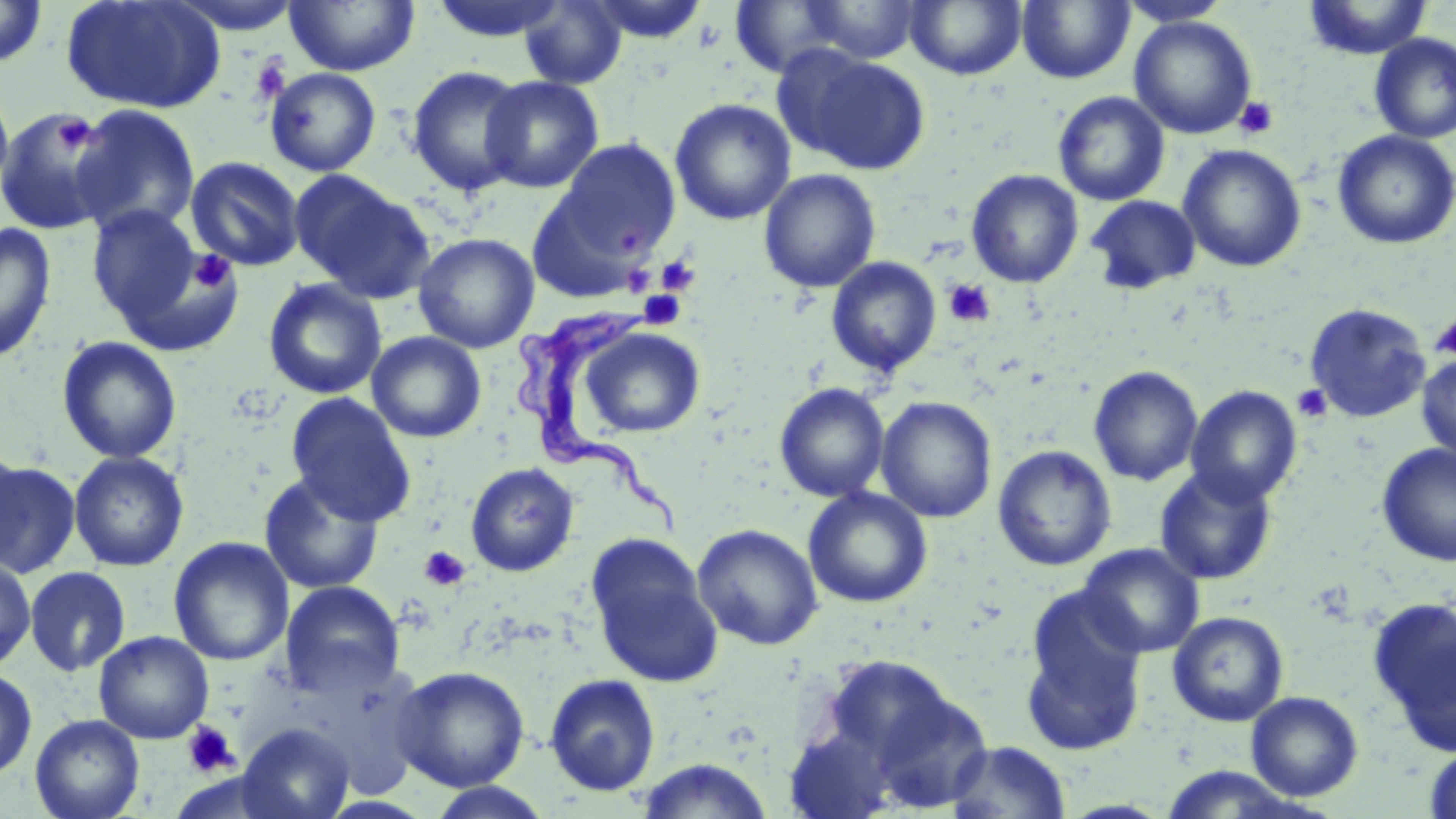
Approximate bounding boxes as [x1, y1, x2, y2] in pixels. Platelet locations: [250, 54, 290, 104], [1234, 96, 1279, 139], [52, 113, 95, 153], [188, 249, 237, 293], [655, 255, 700, 296], [943, 277, 995, 328], [638, 290, 687, 330], [1429, 314, 1456, 360], [1292, 384, 1332, 423], [420, 546, 471, 591], [181, 720, 239, 777]. Uninfected red blood cell locations: [167, 0, 305, 34], [285, 0, 419, 76], [428, 0, 568, 43], [585, 0, 710, 43], [905, 0, 1026, 80], [1116, 0, 1233, 26], [1303, 0, 1433, 60], [0, 1, 48, 68], [61, 1, 225, 115], [519, 1, 627, 89], [800, 1, 924, 63], [1017, 1, 1134, 84], [729, 2, 846, 78], [1129, 15, 1257, 139], [1369, 33, 1456, 143], [792, 50, 930, 175], [406, 65, 529, 197], [265, 67, 381, 176], [479, 75, 604, 193], [0, 80, 14, 203], [1052, 91, 1170, 207], [669, 98, 797, 225], [69, 104, 201, 238], [0, 107, 118, 234], [1333, 130, 1456, 250], [555, 138, 682, 261], [1178, 144, 1307, 272], [185, 156, 305, 271], [758, 169, 881, 293], [291, 170, 436, 304], [966, 170, 1083, 288], [1086, 195, 1201, 295], [86, 206, 222, 339], [0, 222, 58, 364], [413, 232, 540, 353], [826, 256, 942, 377], [263, 278, 387, 400], [1303, 302, 1432, 423], [580, 326, 705, 437], [366, 331, 486, 443], [56, 335, 182, 464], [1415, 352, 1456, 464], [1088, 366, 1203, 486], [773, 382, 890, 502], [1186, 385, 1303, 507], [285, 392, 416, 525], [876, 396, 998, 523], [0, 440, 28, 569], [1377, 442, 1456, 566], [993, 444, 1116, 571], [68, 451, 189, 572], [1, 460, 82, 579], [465, 462, 579, 577], [1153, 465, 1278, 585], [258, 472, 385, 594], [802, 487, 933, 608], [692, 523, 824, 650], [168, 537, 294, 667], [585, 537, 724, 687], [1078, 543, 1205, 658], [0, 556, 36, 672], [24, 566, 131, 677], [280, 580, 405, 698], [1020, 586, 1148, 754], [1367, 596, 1456, 758], [1167, 610, 1290, 727], [93, 630, 214, 744], [392, 665, 530, 791], [0, 667, 37, 780], [544, 673, 661, 796], [1246, 691, 1364, 801], [30, 714, 145, 819], [236, 722, 356, 819], [946, 740, 1072, 819], [1423, 743, 1456, 819], [634, 758, 775, 819], [1154, 767, 1317, 817], [424, 782, 556, 818]. Trypanosoma brucei locations: [513, 306, 687, 537]. Slide-level diagnosis: Trypanosoma brucei. May-Grünwald-Giemsa stain. Image is 1456×819 pixels. Optical microscopy. Thin blood film. One field of a larger specimen. 1000x magnification.